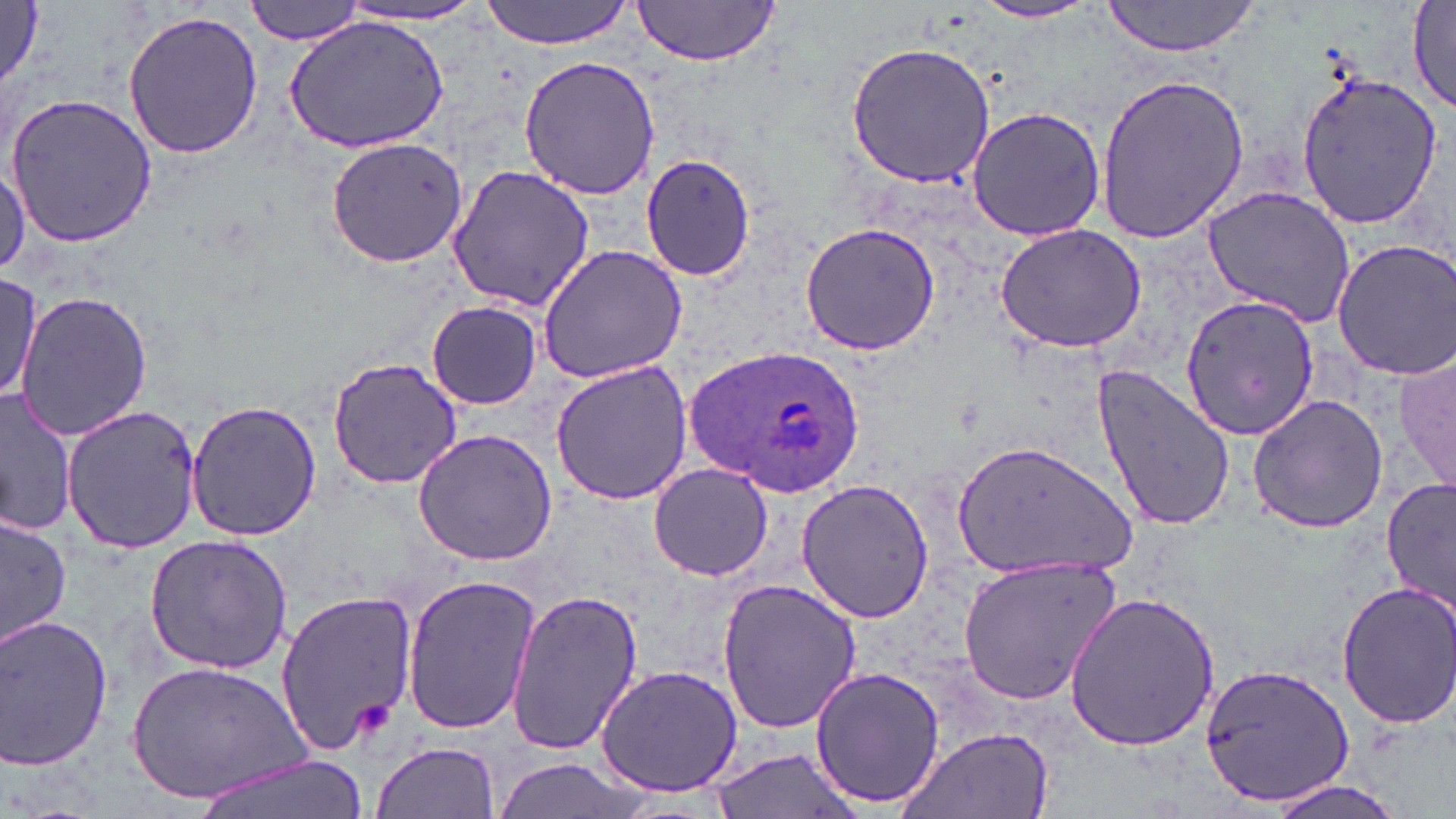

Summary:
  - Coordinate format: approximate bounding boxes as (x1, y1, x2, y2) in pixels
  - Plasmodium ovale-infected red blood cell locations: (689, 344, 866, 497)
  - Uninfected red blood cell locations: (0, 0, 46, 88), (243, 0, 367, 46), (477, 0, 639, 48), (1099, 0, 1265, 58), (1407, 0, 1456, 111), (629, 1, 784, 66), (972, 1, 1102, 23), (329, 4, 492, 30), (121, 9, 263, 161), (284, 15, 448, 150), (846, 41, 997, 188), (519, 55, 661, 199), (1094, 69, 1249, 245), (1295, 70, 1441, 231), (4, 92, 158, 247), (965, 106, 1105, 241), (325, 136, 468, 268), (640, 152, 755, 281), (0, 155, 29, 277), (448, 166, 595, 310), (1202, 185, 1358, 326), (798, 221, 942, 356), (994, 224, 1146, 354), (1331, 238, 1456, 381), (538, 243, 688, 382), (2, 274, 45, 409), (15, 291, 153, 441), (1178, 293, 1319, 441), (426, 300, 543, 410), (1394, 342, 1454, 501), (327, 355, 462, 490), (549, 361, 694, 507), (1091, 361, 1236, 534), (1, 388, 74, 537), (1247, 392, 1389, 532), (186, 400, 321, 543), (62, 403, 201, 556), (413, 429, 558, 566), (954, 440, 1134, 577), (649, 462, 772, 581), (1382, 474, 1455, 615), (796, 478, 936, 623), (0, 512, 72, 653), (143, 534, 295, 676), (956, 555, 1122, 706), (401, 575, 540, 737), (715, 579, 864, 735), (1332, 580, 1456, 731), (274, 589, 420, 756), (505, 589, 645, 754), (1063, 592, 1221, 751), (0, 614, 115, 770), (126, 660, 308, 805), (1201, 662, 1355, 806), (595, 665, 746, 797), (811, 665, 946, 810), (897, 726, 1055, 819), (370, 742, 501, 819), (703, 748, 865, 819), (193, 752, 370, 819), (492, 755, 644, 819), (1259, 775, 1413, 819)
  - Slide-level diagnosis: Plasmodium ovale
  - Modality: optical microscopy
  - Image size: 1456×819 pixels
  - Field of view: one of a larger specimen
  - Stain: May-Grünwald-Giemsa
  - Magnification: 1000x
  - Preparation: thin blood smear